State the blood parasite species.
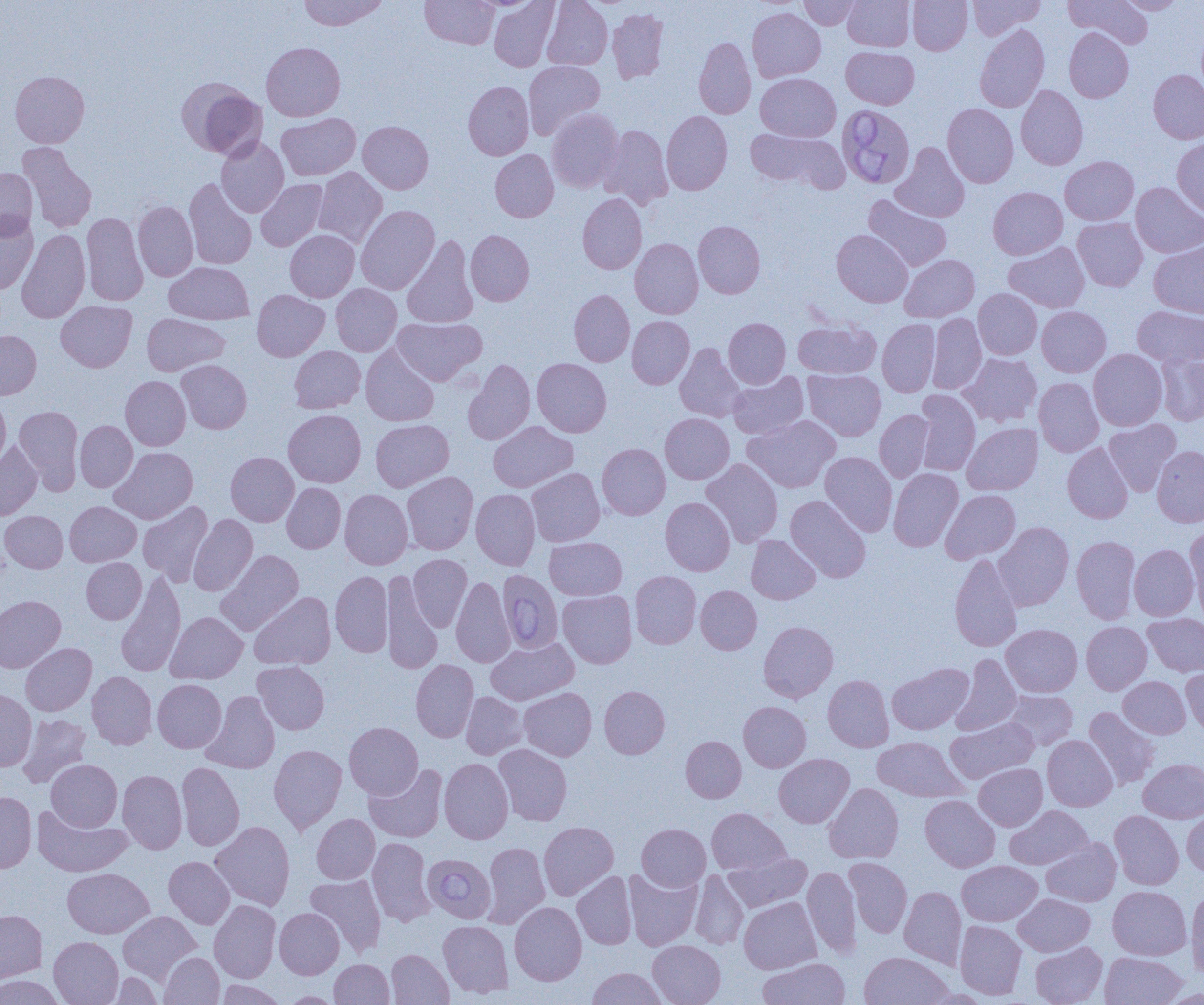

Babesia divergens.

Approximate bounding boxes as (x1, y1, x2, y2) in pixels. Uninfected red blood cell locations: (299, 0, 389, 30), (420, 0, 499, 49), (489, 0, 560, 72), (542, 0, 612, 70), (799, 0, 862, 29), (843, 0, 914, 51), (908, 0, 972, 55), (968, 0, 1045, 39), (1065, 0, 1152, 48), (1117, 1, 1185, 15), (607, 8, 669, 83), (747, 8, 826, 82), (974, 24, 1050, 113), (1064, 27, 1133, 103), (693, 36, 756, 119), (261, 42, 345, 121), (841, 46, 919, 109), (523, 61, 605, 139), (1148, 69, 1204, 144), (10, 71, 89, 147), (756, 73, 840, 142), (176, 77, 267, 159), (463, 81, 534, 160), (1016, 85, 1088, 169), (943, 103, 1018, 188), (546, 108, 624, 193), (661, 111, 732, 195), (277, 113, 360, 180), (358, 121, 433, 194), (600, 124, 673, 209), (745, 128, 848, 193), (216, 137, 289, 217), (1172, 137, 1204, 218), (18, 142, 97, 233), (891, 142, 969, 222), (490, 149, 558, 222), (1060, 156, 1138, 225), (313, 167, 387, 248), (0, 168, 38, 240), (184, 179, 257, 270), (256, 179, 328, 251), (1130, 182, 1204, 257), (988, 186, 1067, 260), (577, 194, 646, 274), (863, 195, 951, 271), (133, 201, 198, 281), (356, 205, 440, 295), (81, 213, 148, 306), (0, 215, 38, 294), (1073, 217, 1147, 291), (693, 220, 765, 298), (16, 229, 90, 324), (285, 229, 359, 302), (465, 229, 534, 306), (832, 229, 913, 307), (402, 235, 479, 328), (630, 238, 703, 319), (1148, 240, 1204, 318), (1003, 242, 1089, 313), (900, 254, 979, 322), (164, 262, 254, 324), (331, 284, 401, 356), (973, 288, 1042, 360), (569, 289, 635, 366), (252, 290, 329, 361), (56, 301, 137, 372), (1037, 306, 1111, 377), (1132, 306, 1204, 367), (142, 313, 229, 376), (927, 313, 986, 394), (392, 316, 485, 385), (627, 316, 694, 389), (723, 317, 790, 388), (877, 319, 940, 397), (793, 320, 880, 379), (0, 330, 41, 400), (674, 343, 745, 422), (289, 346, 365, 413), (360, 346, 439, 426), (1088, 349, 1167, 431), (1156, 351, 1204, 426), (958, 352, 1042, 427), (532, 358, 611, 437), (463, 359, 535, 445), (177, 360, 252, 433), (803, 369, 886, 441), (727, 371, 808, 439), (120, 375, 191, 450), (1034, 377, 1104, 457), (914, 390, 981, 476), (0, 397, 11, 471), (14, 405, 83, 495), (284, 409, 366, 487), (874, 409, 934, 483), (660, 413, 734, 484), (742, 415, 840, 493), (371, 419, 453, 492), (1104, 419, 1181, 496), (75, 420, 137, 492), (488, 421, 578, 492), (962, 422, 1043, 495), (0, 442, 42, 520), (1062, 442, 1132, 523), (597, 443, 670, 520), (1152, 445, 1204, 527), (110, 447, 198, 523), (820, 451, 897, 537), (226, 452, 299, 526), (701, 458, 783, 547), (526, 468, 605, 546), (888, 468, 963, 552), (402, 471, 478, 555), (282, 483, 345, 553), (340, 489, 412, 569), (471, 489, 540, 569), (940, 489, 1020, 563), (785, 495, 871, 583), (660, 497, 735, 576), (65, 501, 141, 566), (137, 501, 213, 586), (1, 511, 68, 573), (188, 514, 258, 595), (994, 522, 1073, 610), (1185, 525, 1204, 615), (746, 535, 820, 604), (1072, 535, 1140, 624), (544, 537, 626, 600), (1129, 544, 1199, 620), (216, 550, 303, 635), (949, 553, 1022, 652), (408, 554, 472, 631), (82, 558, 146, 624), (116, 571, 186, 677), (330, 571, 393, 657), (381, 571, 443, 674), (630, 571, 701, 649), (451, 576, 515, 668), (695, 586, 761, 654), (557, 589, 637, 668), (249, 592, 336, 669), (0, 595, 65, 673), (166, 612, 248, 684), (1143, 613, 1204, 677), (759, 621, 838, 702), (1081, 621, 1151, 694), (1001, 624, 1082, 697), (485, 637, 578, 705), (20, 643, 96, 716), (951, 655, 1022, 736), (411, 660, 479, 742), (253, 661, 329, 734), (887, 663, 973, 735), (1182, 665, 1204, 738), (87, 671, 157, 749), (823, 675, 894, 752), (1118, 676, 1190, 738), (153, 679, 226, 753), (599, 686, 670, 759), (519, 687, 596, 760), (0, 689, 36, 771), (201, 690, 280, 774), (1005, 690, 1078, 750), (461, 691, 527, 759), (739, 702, 811, 772), (1084, 706, 1160, 789), (17, 713, 91, 788), (946, 717, 1039, 783), (344, 722, 423, 800), (1042, 735, 1117, 811), (681, 736, 746, 802), (872, 737, 967, 802), (269, 744, 346, 833), (494, 744, 572, 825), (774, 753, 854, 828), (439, 758, 513, 844), (1138, 758, 1204, 822), (46, 759, 122, 831), (177, 762, 245, 850), (974, 763, 1047, 830), (364, 764, 448, 843), (118, 769, 187, 854), (824, 783, 903, 864), (0, 791, 36, 873), (920, 795, 1000, 872), (1005, 805, 1093, 870), (32, 806, 131, 877), (1182, 807, 1204, 877), (707, 808, 790, 874), (1109, 810, 1184, 890), (312, 814, 380, 884), (210, 821, 295, 910), (539, 821, 618, 900), (637, 823, 710, 891), (367, 837, 436, 926), (1041, 837, 1121, 906), (481, 842, 550, 929), (724, 852, 812, 911), (164, 856, 234, 928), (844, 857, 913, 938), (957, 860, 1042, 926), (803, 866, 860, 957), (62, 868, 154, 938), (624, 868, 702, 950), (690, 870, 748, 949), (572, 872, 637, 949), (305, 874, 386, 956), (1108, 885, 1191, 960), (899, 886, 966, 969), (1186, 887, 1204, 977), (1013, 893, 1095, 956), (739, 897, 821, 973), (209, 900, 281, 982), (510, 901, 586, 985), (274, 908, 344, 979), (0, 909, 47, 983), (118, 911, 202, 985), (438, 920, 513, 997), (955, 921, 1026, 999), (49, 936, 123, 1005), (648, 940, 725, 1005), (1030, 942, 1107, 1005), (387, 949, 453, 1004), (859, 951, 953, 1005), (160, 952, 224, 1004), (1100, 952, 1187, 1005), (758, 958, 850, 1005), (330, 959, 394, 1004), (586, 967, 668, 1005), (109, 972, 163, 1004), (0, 975, 67, 1005), (215, 980, 285, 1005), (280, 991, 343, 1004). Babesia divergens-infected red blood cell locations: (837, 105, 916, 188), (497, 569, 563, 654), (422, 853, 496, 923). Captured at 1000x magnification. Single field of view. Thin blood film. Optical microscopy. Image is 1204×1005 pixels.